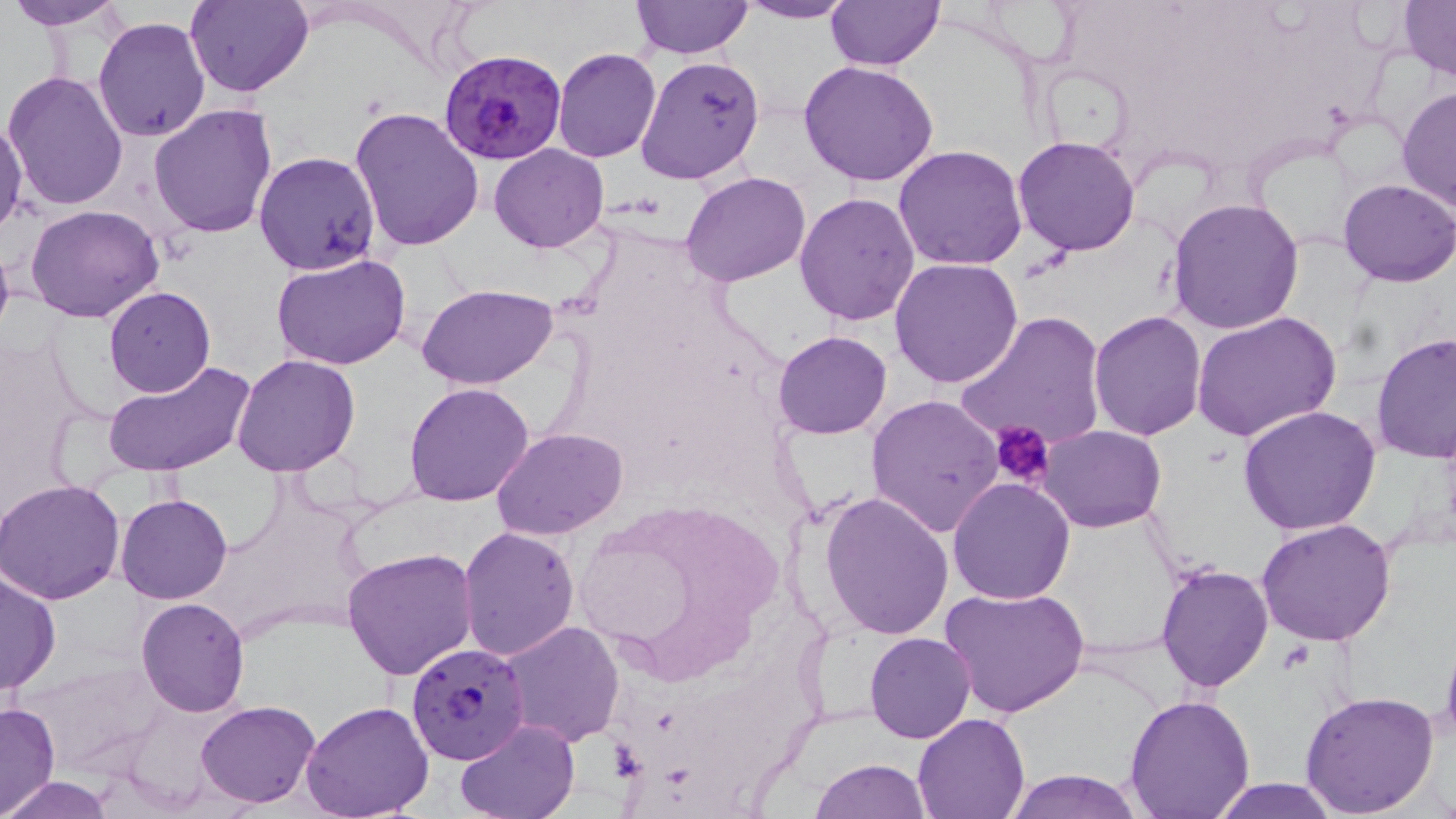 Approximate bounding boxes as [x1, y1, x2, y2] in pixels. Plasmodium falciparum-infected red blood cell locations: [440, 51, 566, 164], [405, 642, 530, 767]. Platelet locations: [992, 419, 1055, 489]. Uninfected red blood cell locations: [5, 0, 127, 29], [185, 0, 313, 97], [733, 0, 860, 23], [824, 0, 946, 71], [630, 1, 753, 58], [1398, 1, 1456, 80], [93, 15, 211, 141], [552, 47, 662, 163], [635, 56, 766, 185], [798, 59, 940, 188], [3, 72, 129, 212], [1396, 85, 1455, 216], [148, 101, 278, 236], [350, 105, 484, 253], [0, 117, 26, 235], [1013, 136, 1141, 256], [895, 143, 1028, 270], [489, 144, 610, 253], [253, 152, 381, 275], [681, 172, 812, 287], [1338, 178, 1456, 286], [794, 191, 922, 325], [1165, 198, 1305, 335], [24, 205, 164, 323], [0, 234, 15, 347], [269, 251, 411, 371], [891, 259, 1024, 389], [417, 284, 559, 389], [103, 286, 215, 397], [956, 311, 1107, 453], [1088, 311, 1206, 440], [1191, 312, 1340, 444], [773, 331, 892, 440], [1371, 331, 1456, 463], [231, 353, 361, 478], [101, 359, 257, 480], [403, 382, 534, 505], [866, 393, 1003, 539], [1239, 406, 1383, 536], [1039, 423, 1166, 531], [492, 428, 628, 539], [0, 479, 128, 603], [948, 479, 1076, 604], [818, 491, 955, 639], [116, 493, 232, 603], [1257, 519, 1397, 647], [458, 527, 580, 661], [340, 548, 480, 681], [1156, 563, 1273, 692], [0, 566, 60, 696], [940, 586, 1090, 721], [136, 599, 249, 717], [497, 620, 624, 746], [1439, 630, 1456, 751], [866, 632, 975, 742], [1299, 689, 1440, 815], [1122, 695, 1257, 816], [194, 698, 321, 807], [301, 699, 435, 819], [0, 701, 60, 817], [912, 713, 1030, 819], [453, 719, 582, 818], [809, 758, 930, 819], [1004, 768, 1147, 819], [2, 776, 114, 818], [1203, 778, 1347, 818]. Slide-level diagnosis: Plasmodium falciparum. Thin blood smear. Image is 1456×819 pixels. May-Grünwald-Giemsa stain. Single field of view. Optical microscopy. 1000x magnification.